Name the blood parasite species.
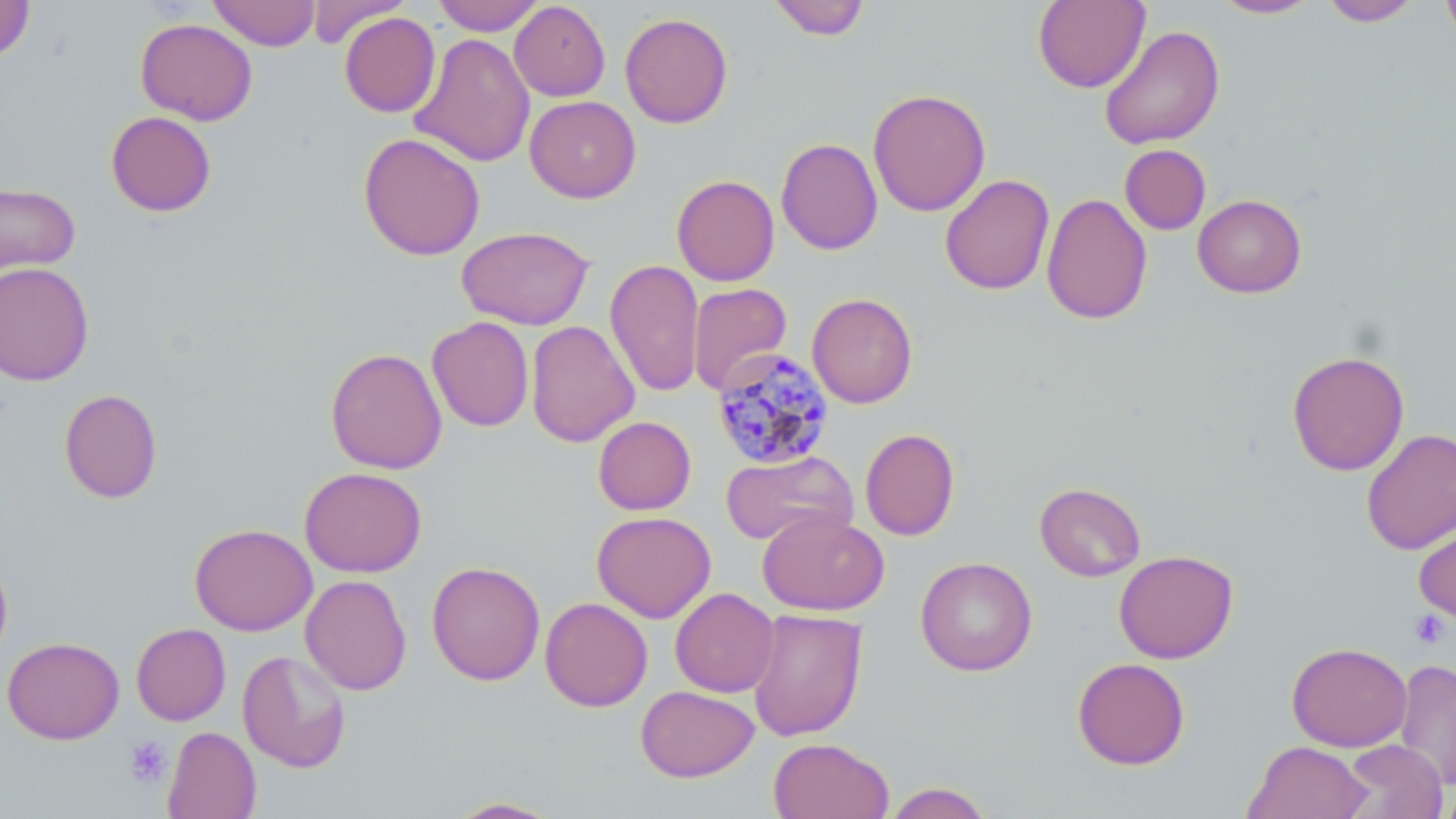
Plasmodium malariae.

Summary:
  - Coordinate format: approximate bounding boxes as [x1, y1, x2, y2] in pixels
  - Plasmodium malariae-infected red blood cell locations: [711, 346, 834, 470]
  - Uninfected red blood cell locations: [0, 0, 34, 63], [208, 0, 321, 51], [305, 0, 410, 48], [432, 0, 545, 35], [767, 0, 871, 41], [1210, 0, 1321, 19], [1440, 0, 1456, 51], [509, 1, 611, 101], [1033, 1, 1150, 93], [1318, 1, 1424, 27], [339, 12, 441, 118], [619, 13, 733, 128], [135, 18, 258, 125], [1098, 25, 1225, 150], [409, 32, 536, 168], [868, 88, 991, 217], [525, 95, 641, 203], [105, 111, 216, 216], [358, 133, 486, 260], [776, 138, 883, 255], [1120, 144, 1211, 235], [939, 174, 1054, 295], [672, 175, 780, 286], [0, 182, 80, 276], [1041, 193, 1153, 325], [1192, 194, 1307, 298], [456, 225, 595, 330], [605, 259, 705, 397], [0, 261, 94, 386], [688, 283, 792, 396], [807, 293, 918, 409], [427, 316, 534, 432], [525, 320, 640, 447], [325, 348, 447, 474], [1287, 350, 1410, 476], [59, 389, 162, 503], [593, 416, 696, 515], [1361, 427, 1456, 556], [860, 428, 960, 540], [721, 450, 858, 547], [299, 467, 427, 577], [1034, 482, 1146, 581], [591, 511, 716, 623], [757, 511, 889, 616], [1414, 518, 1456, 628], [189, 523, 318, 636], [1114, 550, 1238, 664], [0, 551, 13, 666], [915, 556, 1037, 677], [427, 560, 546, 686], [299, 575, 412, 696], [670, 588, 779, 697], [540, 596, 653, 712], [746, 608, 869, 742], [131, 623, 231, 725], [2, 636, 124, 743], [1287, 642, 1412, 752], [238, 649, 351, 773], [1072, 657, 1190, 770], [1393, 658, 1456, 790], [635, 685, 759, 782], [163, 726, 261, 819], [768, 738, 895, 819], [1338, 739, 1448, 819], [1243, 741, 1373, 819], [882, 782, 994, 819], [1436, 783, 1456, 819], [444, 796, 567, 818]
  - Platelet locations: [1408, 610, 1450, 649], [124, 737, 171, 788]
  - Image size: 1456×819 pixels
  - Field of view: one of a larger specimen
  - Modality: optical microscopy
  - Stain: May-Grünwald-Giemsa
  - Preparation: thin blood film
  - Magnification: 1000x